State the preparation type.
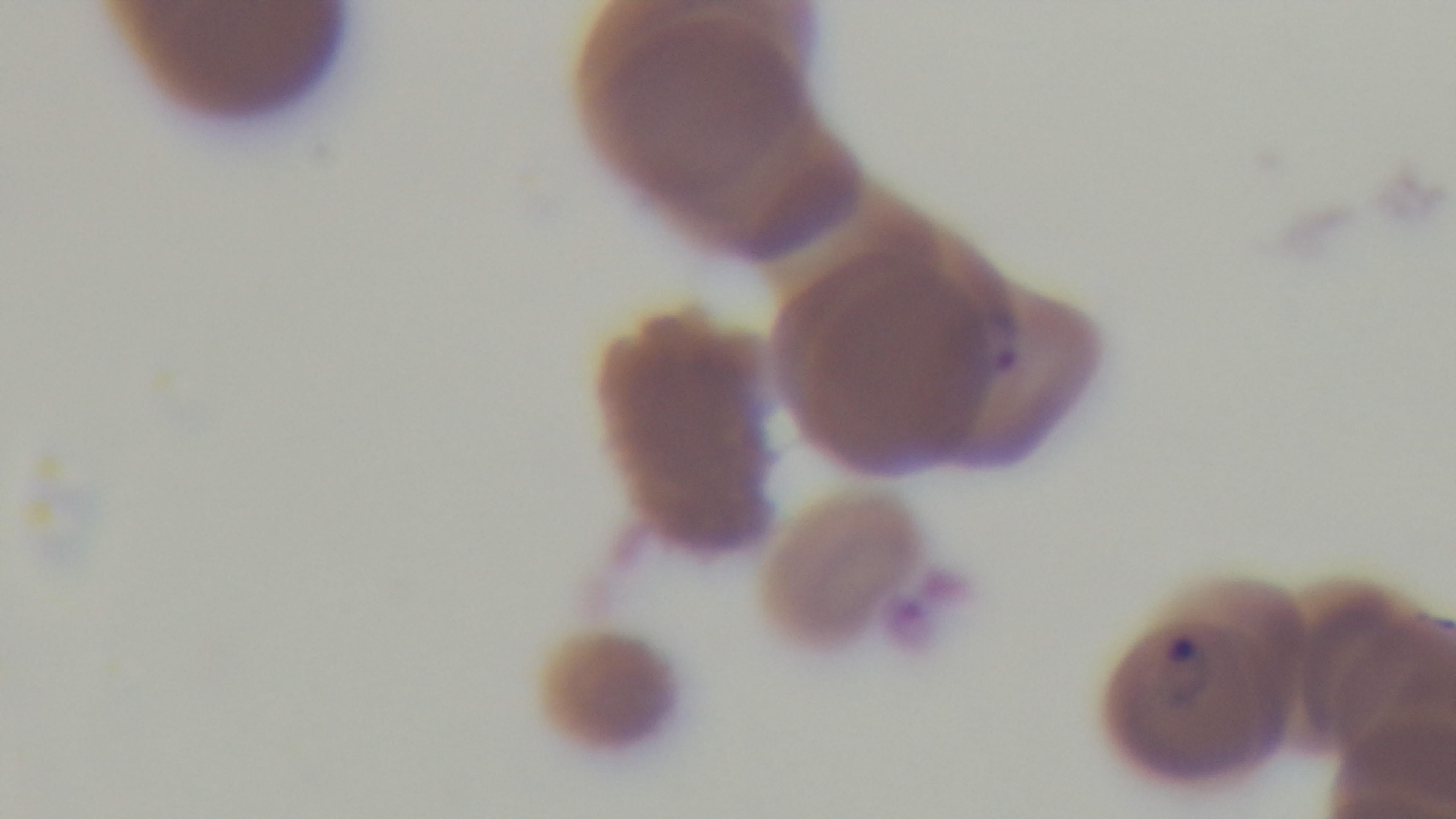

Thin.

{
  "field_of_view": "single",
  "stain": "Giemsa",
  "modality": "light microscopy",
  "malaria_status": "positive",
  "capture": "mounted 4K digital camera",
  "objective": "100x oil immersion"
}